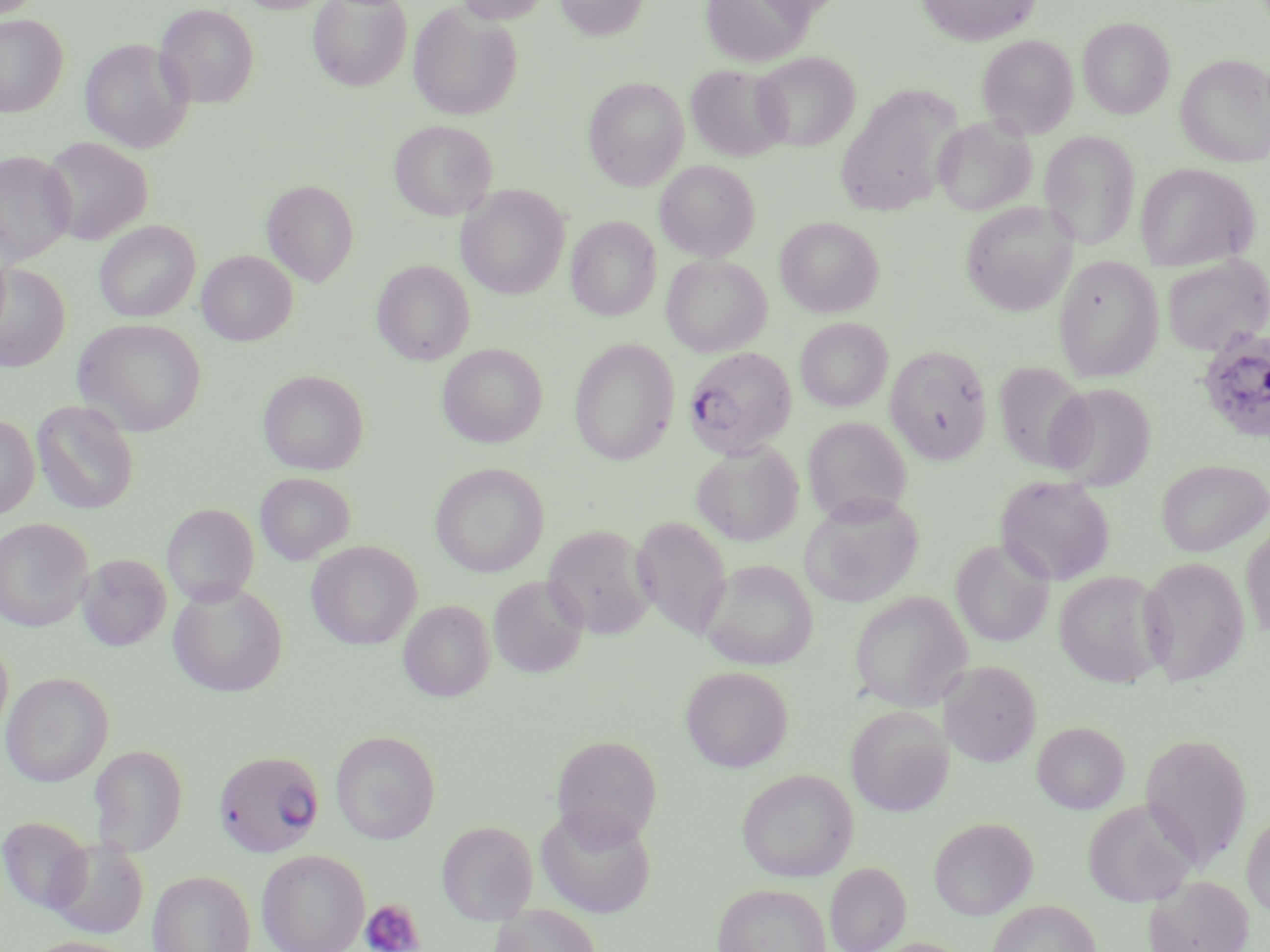
slide-level diagnosis = Plasmodium falciparum
platelet locations = approximate bounding boxes as [x1, y1, x2, y2] in pixels: [360, 899, 424, 952]
modality = optical microscopy
magnification = 1000x
stain = May-Grünwald-Giemsa
field of view = one of a larger specimen
preparation = thin blood smear
Plasmodium falciparum-infected red blood cell locations = approximate bounding boxes as [x1, y1, x2, y2] in pixels: [1196, 327, 1270, 444], [683, 347, 797, 460], [213, 750, 325, 858]
uninfected red blood cell locations = approximate bounding boxes as [x1, y1, x2, y2] in pixels: [235, 0, 336, 13], [308, 0, 412, 91], [453, 0, 552, 25], [554, 0, 649, 40], [700, 0, 813, 68], [917, 0, 1041, 46], [408, 2, 523, 121], [154, 3, 259, 108], [0, 14, 68, 117], [1078, 17, 1174, 118], [977, 35, 1079, 139], [80, 38, 194, 153], [753, 52, 859, 150], [1176, 54, 1270, 166], [686, 64, 791, 162], [583, 77, 689, 190], [834, 83, 965, 216], [933, 115, 1038, 216], [389, 120, 497, 220], [1039, 130, 1140, 251], [39, 137, 153, 246], [0, 149, 77, 267], [655, 160, 760, 261], [1134, 163, 1260, 271], [262, 180, 360, 287], [457, 184, 570, 299], [960, 201, 1079, 315], [566, 216, 662, 321], [775, 216, 884, 317], [94, 221, 200, 322], [197, 250, 298, 345], [1161, 253, 1269, 356], [661, 254, 772, 356], [1053, 255, 1163, 382], [373, 260, 474, 365], [1, 264, 70, 372], [795, 317, 893, 412], [72, 318, 206, 436], [569, 337, 680, 465], [437, 344, 547, 448], [886, 346, 992, 465], [994, 361, 1092, 473], [258, 370, 369, 475], [1046, 382, 1156, 491], [32, 400, 140, 515], [0, 414, 39, 519], [803, 416, 912, 524], [692, 443, 803, 546], [1156, 458, 1270, 557], [430, 462, 549, 577], [255, 472, 354, 565], [995, 475, 1116, 586], [799, 493, 924, 607], [162, 503, 259, 606], [631, 516, 732, 639], [0, 518, 94, 631], [543, 524, 657, 639], [1241, 525, 1270, 641], [951, 539, 1054, 647], [306, 540, 423, 650], [76, 553, 171, 652], [1138, 557, 1249, 687], [698, 559, 817, 669], [1053, 570, 1170, 688], [488, 575, 588, 677], [168, 581, 288, 697], [849, 591, 972, 712], [398, 599, 494, 702], [0, 636, 13, 740], [941, 660, 1041, 766], [680, 666, 793, 772], [1, 671, 114, 787], [846, 705, 953, 816], [1032, 721, 1130, 813], [331, 730, 440, 844], [1139, 731, 1253, 870], [551, 734, 662, 845], [87, 744, 188, 856], [735, 767, 858, 882], [1082, 798, 1199, 907], [535, 803, 657, 919], [1241, 813, 1270, 919], [1, 815, 92, 914], [928, 816, 1038, 920], [437, 820, 538, 924], [47, 837, 148, 938], [257, 849, 370, 952], [825, 862, 911, 952], [147, 870, 256, 952], [1145, 875, 1253, 952], [712, 883, 831, 952], [987, 900, 1101, 952], [490, 904, 602, 952], [20, 936, 143, 952], [861, 937, 972, 952]
image size = 1270×952 pixels